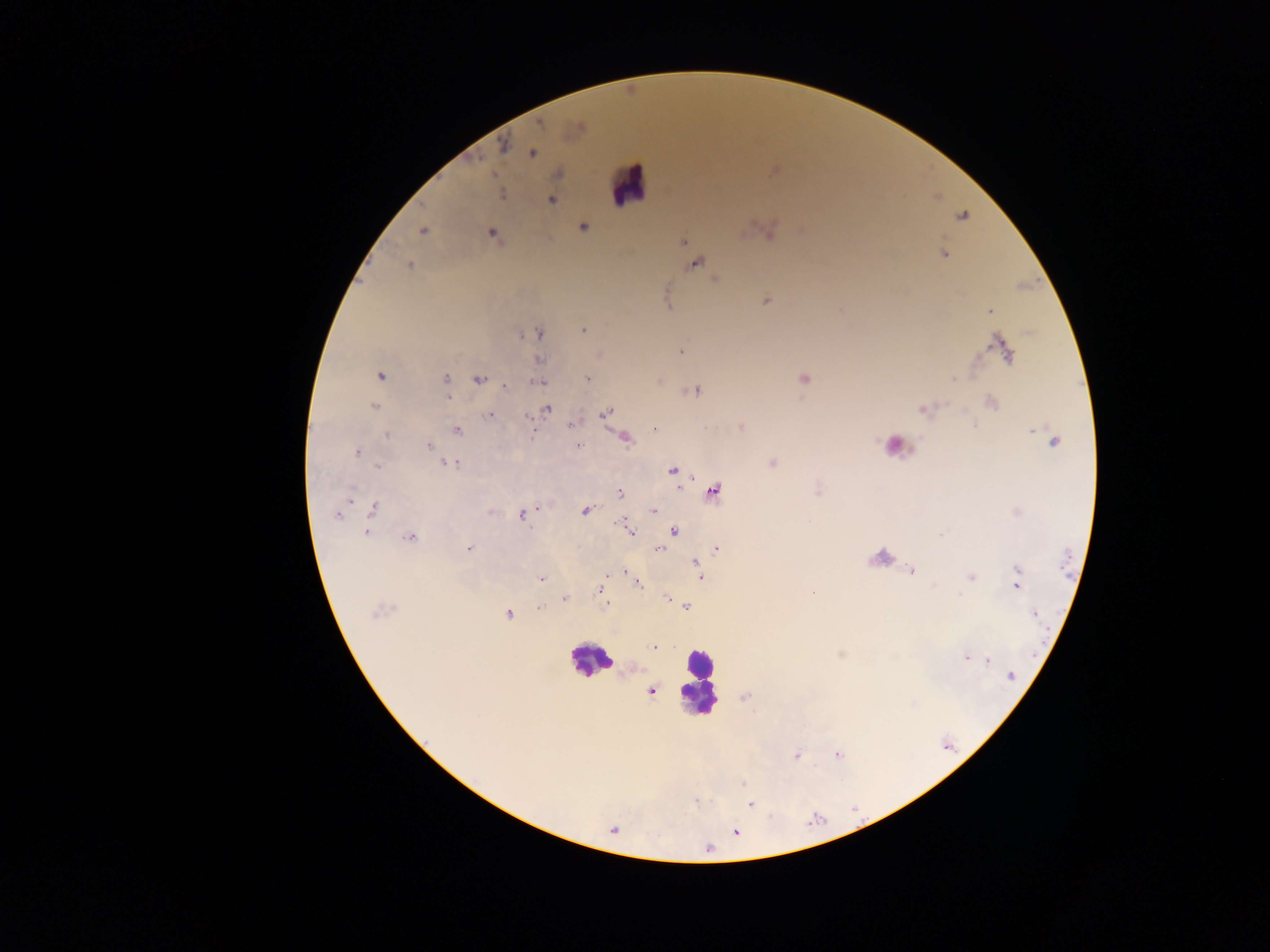
Approximate centers as [x, y] in pixels.
Summary:
  - Leukocyte locations: [628, 186], [896, 442], [590, 660], [698, 682]
  - Plasmodium parasite locations: [539, 124], [503, 145], [532, 153], [501, 194], [551, 200], [583, 227], [423, 231], [492, 234], [683, 241], [944, 254], [697, 263], [409, 265], [715, 279], [765, 301], [990, 311], [583, 330], [539, 334], [1003, 347], [681, 352], [539, 360], [379, 375], [587, 378], [804, 378], [445, 379], [478, 380], [539, 382], [506, 386], [696, 391], [447, 396], [990, 403], [375, 406], [547, 409], [605, 413], [490, 415], [571, 423], [741, 428], [532, 429], [654, 429], [457, 431], [387, 435], [625, 438], [1052, 439], [429, 446], [577, 446], [357, 452], [773, 463], [452, 465], [379, 467], [672, 470], [714, 490], [620, 493], [351, 498], [373, 509], [584, 510], [654, 511], [521, 515], [336, 516], [674, 531], [366, 532], [631, 532], [409, 538], [469, 548], [716, 549], [658, 550], [696, 563], [911, 570], [624, 571], [700, 577], [972, 577], [541, 579], [1017, 580], [639, 584], [600, 590], [667, 598], [565, 599], [606, 604], [687, 606], [539, 609], [380, 611], [508, 614], [1035, 614], [654, 648], [967, 657], [988, 660], [1012, 676], [652, 691], [796, 755], [837, 755], [743, 783], [750, 804], [735, 832], [709, 848]
  - Image size: 1270×952 pixels
  - Country: Ghana
  - Field of view: single
  - Preparation: thick blood smear
  - Capture: mobile-phone photograph through a microscope